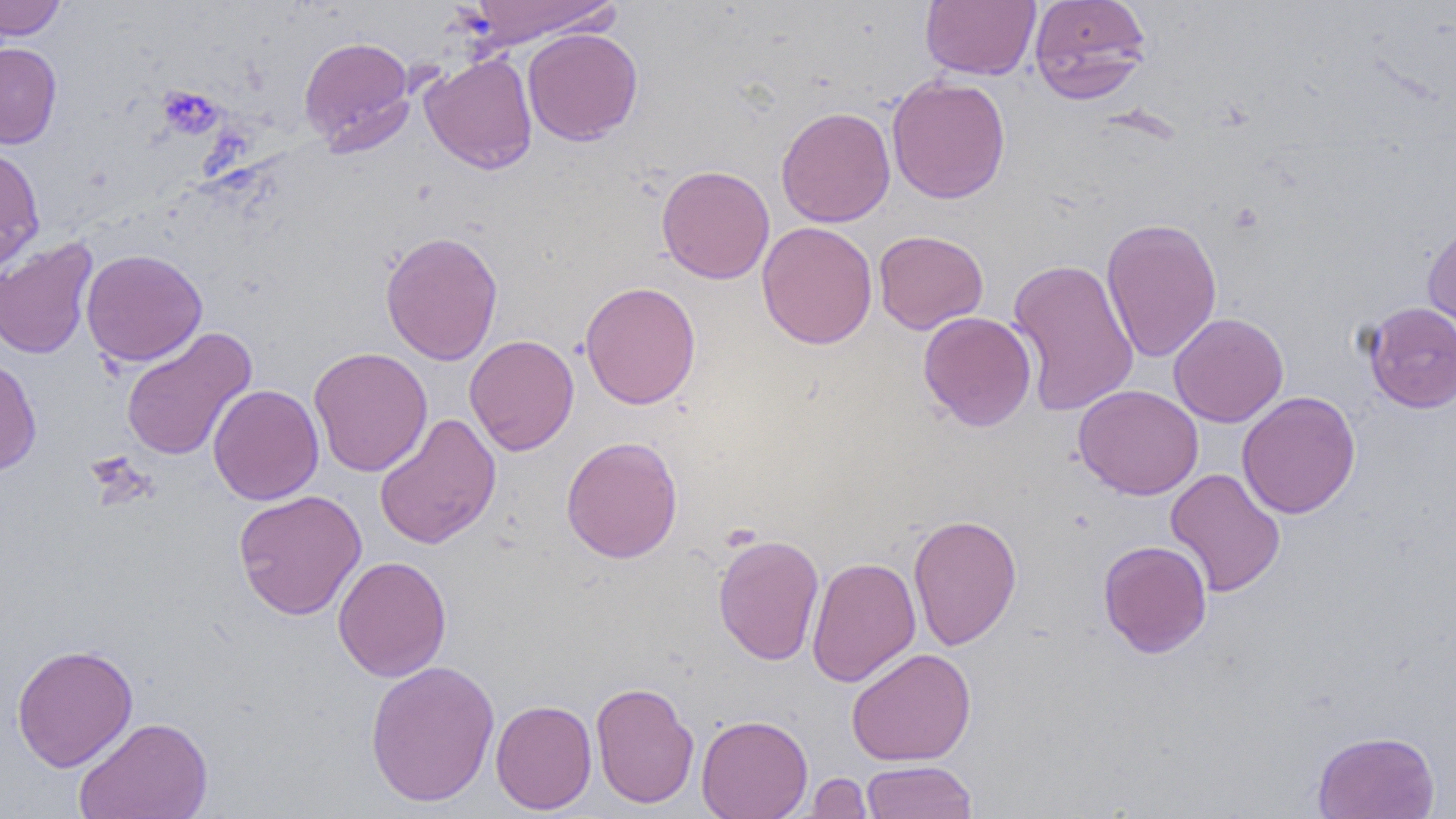
Summary:
  - Coordinate format: approximate bounding boxes as [x1, y1, x2, y2] in pixels
  - Platelet locations: [158, 84, 224, 139], [85, 451, 157, 510]
  - Uninfected red blood cell locations: [0, 0, 67, 40], [464, 0, 621, 48], [921, 0, 1040, 81], [1029, 0, 1152, 103], [522, 27, 643, 145], [298, 36, 416, 154], [0, 42, 62, 149], [420, 53, 538, 174], [886, 75, 1011, 204], [776, 106, 895, 227], [0, 147, 45, 274], [656, 165, 774, 284], [1101, 217, 1222, 363], [1422, 218, 1456, 345], [757, 221, 877, 349], [379, 230, 503, 365], [873, 230, 988, 334], [0, 236, 99, 360], [80, 248, 207, 366], [1007, 257, 1140, 417], [580, 280, 701, 410], [1033, 298, 1165, 483], [1362, 301, 1456, 412], [918, 311, 1037, 432], [1169, 312, 1289, 427], [120, 327, 257, 461], [464, 334, 579, 455], [308, 347, 433, 477], [0, 357, 42, 475], [208, 375, 432, 488], [1073, 384, 1203, 500], [207, 385, 324, 505], [1237, 390, 1361, 519], [374, 413, 502, 549], [561, 436, 684, 563], [1165, 468, 1285, 597], [232, 489, 366, 620], [907, 513, 1023, 650], [712, 532, 825, 666], [1097, 539, 1212, 658], [332, 556, 451, 682], [806, 556, 921, 687], [12, 643, 138, 771], [846, 648, 976, 766], [365, 659, 500, 807], [589, 681, 700, 809], [491, 699, 597, 815], [696, 714, 813, 819], [73, 715, 213, 819], [1312, 730, 1440, 819], [860, 760, 978, 819], [803, 772, 873, 818]
  - Slide-level diagnosis: no evidence of blood parasites
  - Preparation: thin blood smear
  - Field of view: single
  - Magnification: 1000x
  - Image size: 1456×819 pixels
  - Modality: light microscopy